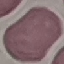 Malaria status: uninfected. Giemsa-stained preparation. Cell patch, automatically extracted from a larger field of view and resized to 64 × 64 pixels. Thin blood film. Acquired by smartphone through the microscope eyepiece.